Give a bounding box for every leukocyte visible.
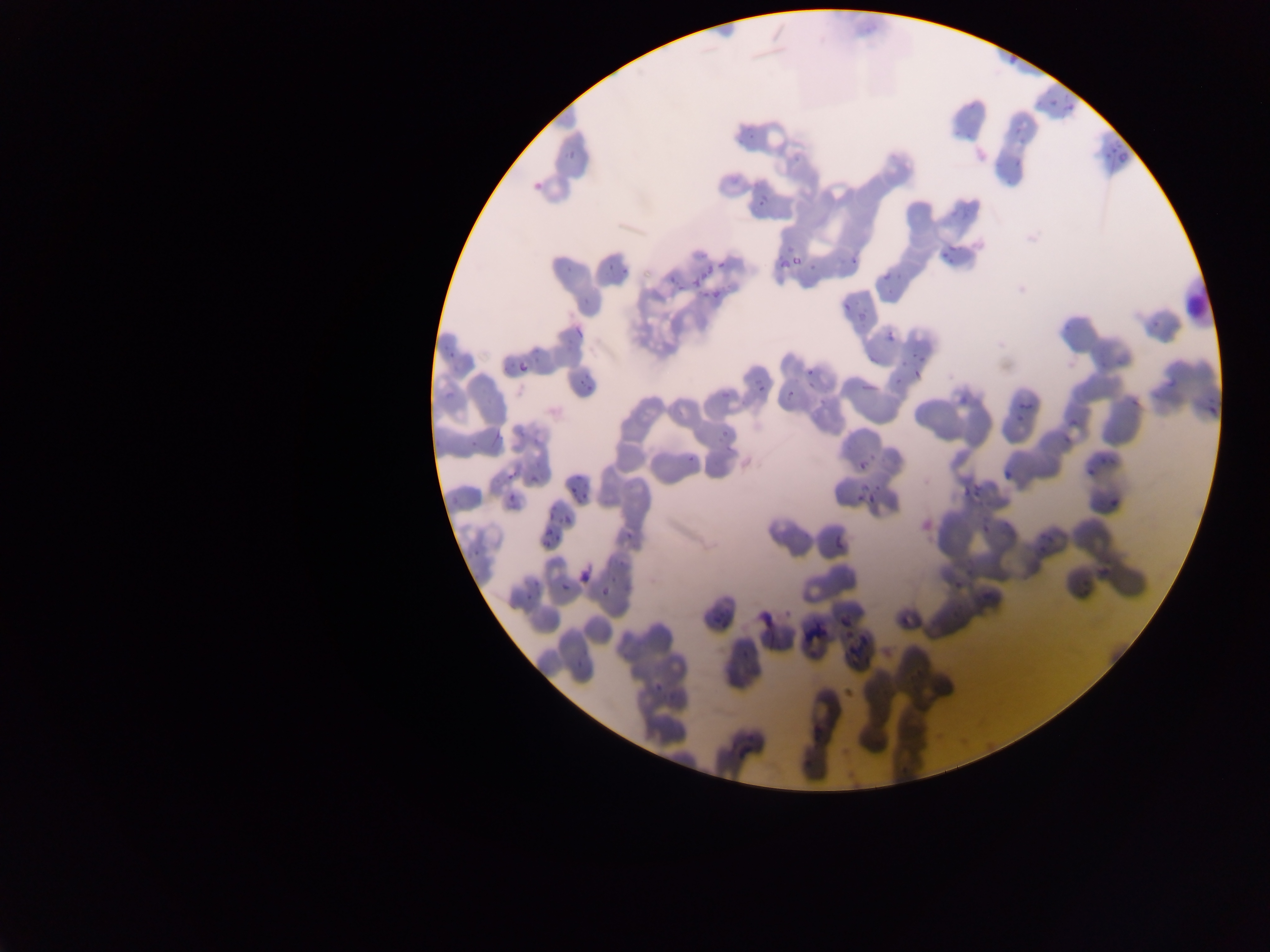

No leukocytes observed.

Approximate bounding boxes as [left, top, right, bottom] in pixels. Malaria parasite locations: [1002, 48, 1023, 71], [1039, 95, 1060, 108], [1057, 100, 1082, 114], [1007, 126, 1028, 145], [1105, 145, 1131, 168], [1010, 158, 1030, 171], [530, 177, 547, 195], [749, 189, 774, 208], [848, 243, 866, 264], [935, 243, 957, 265], [791, 247, 812, 271], [771, 249, 796, 271], [714, 258, 730, 275], [599, 261, 618, 277], [559, 264, 583, 281], [684, 270, 703, 293], [881, 270, 901, 282], [706, 289, 726, 303], [839, 300, 854, 316], [854, 310, 871, 323], [884, 329, 900, 346], [560, 334, 575, 346], [443, 339, 460, 357], [515, 354, 538, 374], [908, 367, 922, 379], [808, 368, 818, 382], [574, 372, 599, 388], [750, 372, 762, 396], [1160, 375, 1183, 398], [780, 380, 799, 396], [1013, 386, 1038, 412], [714, 387, 732, 399], [956, 401, 969, 410], [1203, 408, 1219, 423], [1056, 424, 1080, 444], [485, 425, 506, 444], [714, 430, 730, 440], [684, 449, 699, 468], [851, 456, 876, 472], [1081, 459, 1100, 480], [998, 460, 1020, 482], [504, 472, 519, 482], [569, 480, 584, 492], [506, 484, 521, 501], [962, 486, 982, 502], [856, 488, 884, 505], [1102, 490, 1122, 520], [540, 508, 558, 522], [560, 509, 582, 528], [982, 520, 997, 534], [1031, 527, 1058, 552], [622, 528, 642, 542], [830, 529, 849, 553], [538, 530, 556, 548], [1084, 566, 1110, 587], [577, 567, 593, 585], [520, 579, 538, 602], [559, 581, 572, 593], [954, 581, 967, 592], [596, 585, 612, 601], [970, 598, 998, 615], [758, 609, 784, 633], [709, 613, 725, 627], [837, 613, 853, 633], [800, 627, 822, 646], [842, 633, 865, 657], [731, 643, 752, 666], [651, 678, 670, 697], [807, 721, 821, 738], [730, 739, 758, 761]. Single field of view. Sample from Ghana. Photographed through a microscope with a mobile-phone camera. Thin blood film. Image is 1270×952 pixels.